Identify the blood parasite species.
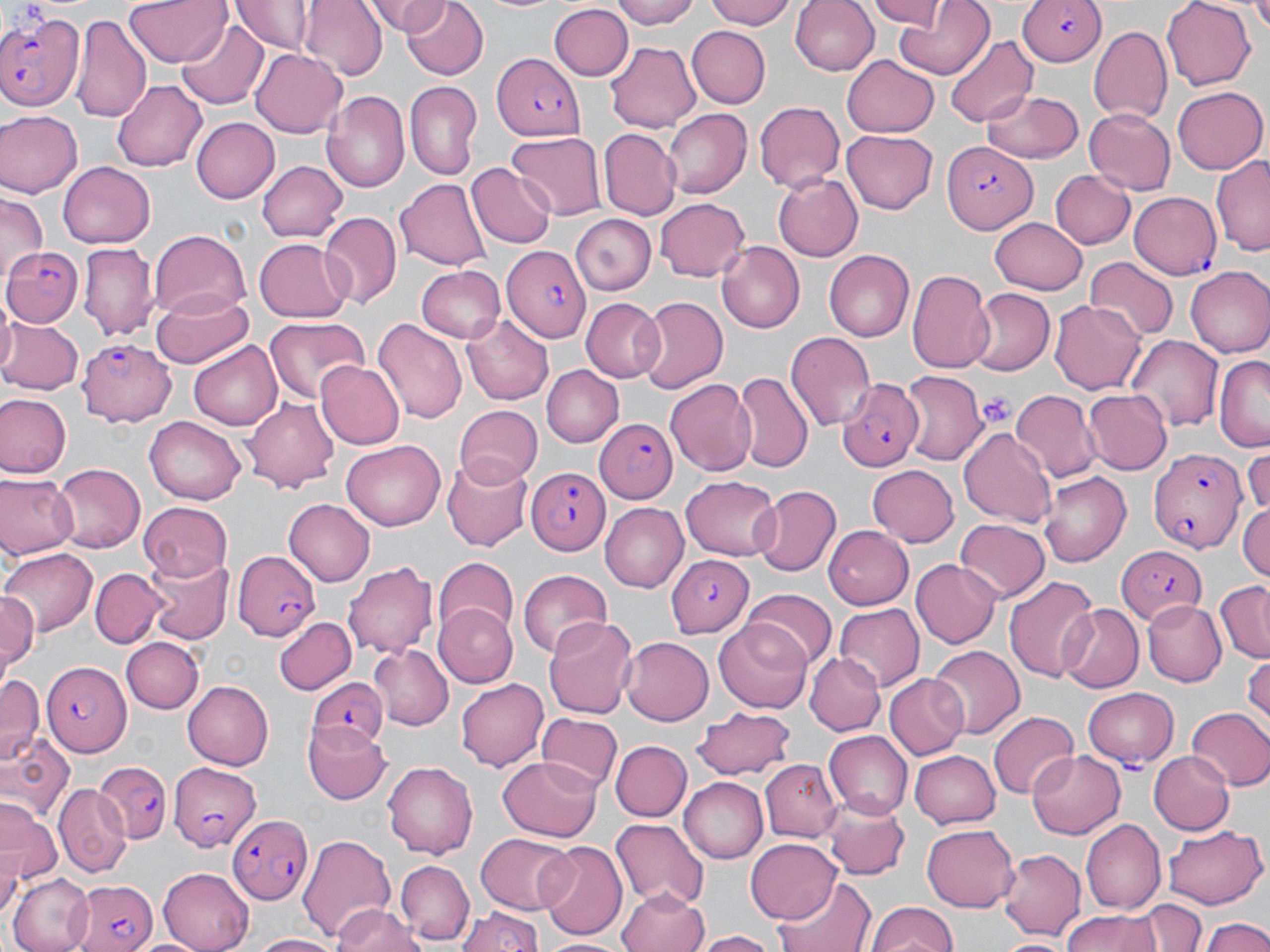
Plasmodium falciparum.

preparation = thin blood smear
Plasmodium falciparum-infected red blood cell locations = approximate bounding boxes as (x1,y1)-(x2,y2) corner pairs in pixels: (1020,0)-(1106,70), (0,6)-(85,113), (491,52)-(582,140), (942,143)-(1039,232), (1129,191)-(1223,279), (1,245)-(82,327), (499,245)-(590,340), (78,340)-(178,428), (837,375)-(926,472), (595,417)-(677,503), (1149,446)-(1249,554), (525,466)-(608,555), (1115,546)-(1210,625), (229,552)-(321,639), (664,555)-(752,635), (43,659)-(129,756), (310,675)-(387,746), (1082,688)-(1179,769), (166,760)-(261,850), (95,762)-(171,845), (231,811)-(312,906), (67,876)-(159,952)
image size = 1270×952 pixels
platelet locations = approximate bounding boxes as (x1,y1)-(x2,y2) corner pairs in pixels: (983,393)-(1016,430)
modality = optical microscopy
uninfected red blood cell locations = approximate bounding boxes as (x1,y1)-(x2,y2) corner pairs in pixels: (124,0)-(231,67), (232,0)-(316,55), (299,0)-(385,81), (366,0)-(451,34), (400,0)-(487,80), (613,0)-(706,29), (706,0)-(802,28), (790,0)-(878,77), (865,0)-(949,29), (1162,0)-(1257,90), (1247,0)-(1270,37), (893,1)-(995,77), (549,5)-(632,80), (74,14)-(150,123), (176,15)-(268,107), (684,25)-(770,110), (1090,25)-(1173,124), (946,35)-(1038,127), (605,39)-(701,134), (251,48)-(347,138), (842,55)-(939,137), (114,78)-(206,173), (405,80)-(482,180), (1173,87)-(1265,174), (981,89)-(1086,166), (322,90)-(410,191), (752,100)-(845,195), (1084,107)-(1176,196), (662,108)-(751,199), (0,110)-(79,198), (192,118)-(279,203), (599,129)-(680,218), (840,130)-(939,214), (507,132)-(606,219), (1210,154)-(1270,256), (256,160)-(348,240), (57,162)-(154,249), (466,163)-(556,248), (772,172)-(862,263), (1051,172)-(1134,249), (396,175)-(491,270), (0,193)-(45,285), (653,197)-(750,282), (319,211)-(401,309), (568,214)-(658,296), (991,217)-(1089,294), (150,231)-(250,324), (253,238)-(352,324), (716,242)-(806,333), (80,244)-(158,343), (823,249)-(914,342), (1086,258)-(1179,341), (415,266)-(507,344), (1184,266)-(1270,357), (907,270)-(997,372), (151,288)-(255,369), (968,289)-(1053,376), (635,296)-(728,395), (580,298)-(665,382), (1049,301)-(1146,395), (462,314)-(557,404), (0,317)-(82,395), (263,317)-(368,406), (372,317)-(466,426), (787,331)-(877,431), (1124,334)-(1225,432), (189,340)-(285,430), (1213,353)-(1270,450), (314,359)-(404,450), (540,365)-(623,448), (734,371)-(813,476), (900,372)-(986,467), (664,376)-(756,477), (1010,389)-(1102,480), (1083,390)-(1172,474), (0,392)-(70,478), (244,394)-(341,488), (454,404)-(542,486), (143,417)-(247,505), (959,426)-(1057,526), (341,441)-(447,531), (1243,446)-(1270,514), (441,454)-(533,552), (52,462)-(147,550), (867,464)-(958,546), (1038,471)-(1132,568), (0,473)-(77,561), (681,477)-(783,563), (750,485)-(841,578), (285,499)-(374,585), (1238,500)-(1270,583), (137,501)-(231,581), (599,502)-(688,594), (954,518)-(1049,602), (822,525)-(915,608), (0,545)-(97,638), (143,554)-(229,646), (433,559)-(518,639), (912,559)-(1001,649), (345,560)-(436,661), (92,567)-(165,647), (518,569)-(612,657), (1004,574)-(1101,684), (1213,581)-(1270,664), (743,589)-(835,671), (1,590)-(40,678), (1140,598)-(1227,687), (1057,602)-(1143,692), (436,603)-(521,685), (834,605)-(924,690), (273,615)-(356,695), (544,615)-(640,719), (711,620)-(814,710), (620,636)-(714,724), (123,637)-(202,712), (368,644)-(454,730), (927,644)-(1026,739), (805,654)-(884,735), (1244,657)-(1270,729), (885,673)-(969,757), (0,676)-(42,767), (454,678)-(549,771), (182,680)-(273,769), (1186,708)-(1270,791), (692,709)-(799,779), (988,710)-(1077,799), (535,714)-(621,796), (302,722)-(391,804), (822,731)-(912,818), (4,735)-(73,822), (611,742)-(691,822), (1027,746)-(1124,837), (910,750)-(1002,830), (1149,752)-(1234,835), (496,755)-(603,842), (760,758)-(842,840), (382,762)-(479,859), (678,776)-(768,864), (54,786)-(127,876), (822,800)-(910,881), (1,805)-(59,890), (610,818)-(708,910), (1080,819)-(1165,914), (922,824)-(1019,911), (1163,826)-(1264,908), (298,832)-(397,942), (474,833)-(577,915), (745,837)-(844,924), (537,840)-(626,939), (998,846)-(1084,940), (397,860)-(475,946), (160,865)-(257,952), (9,873)-(95,952), (772,877)-(876,952), (615,885)-(711,952), (1140,899)-(1205,952), (866,902)-(958,952), (333,905)-(425,951), (457,906)-(544,952), (1059,910)-(1157,952), (1199,916)-(1269,952), (694,929)-(784,951), (247,932)-(346,952), (538,934)-(631,951), (997,937)-(1073,952)
stain = May-Grünwald-Giemsa
field of view = one of a larger specimen
magnification = 1000x